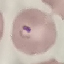
malaria status = parasitized
capture = smartphone camera at the microscope eyepiece
image type = automatically extracted cell patch, resized to 64 × 64 pixels
stain = Giemsa
preparation = thin blood smear